Identify the cell.
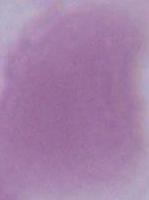
An erythrocyte.

{
  "modality": "micrograph",
  "magnification": "1000x"
}